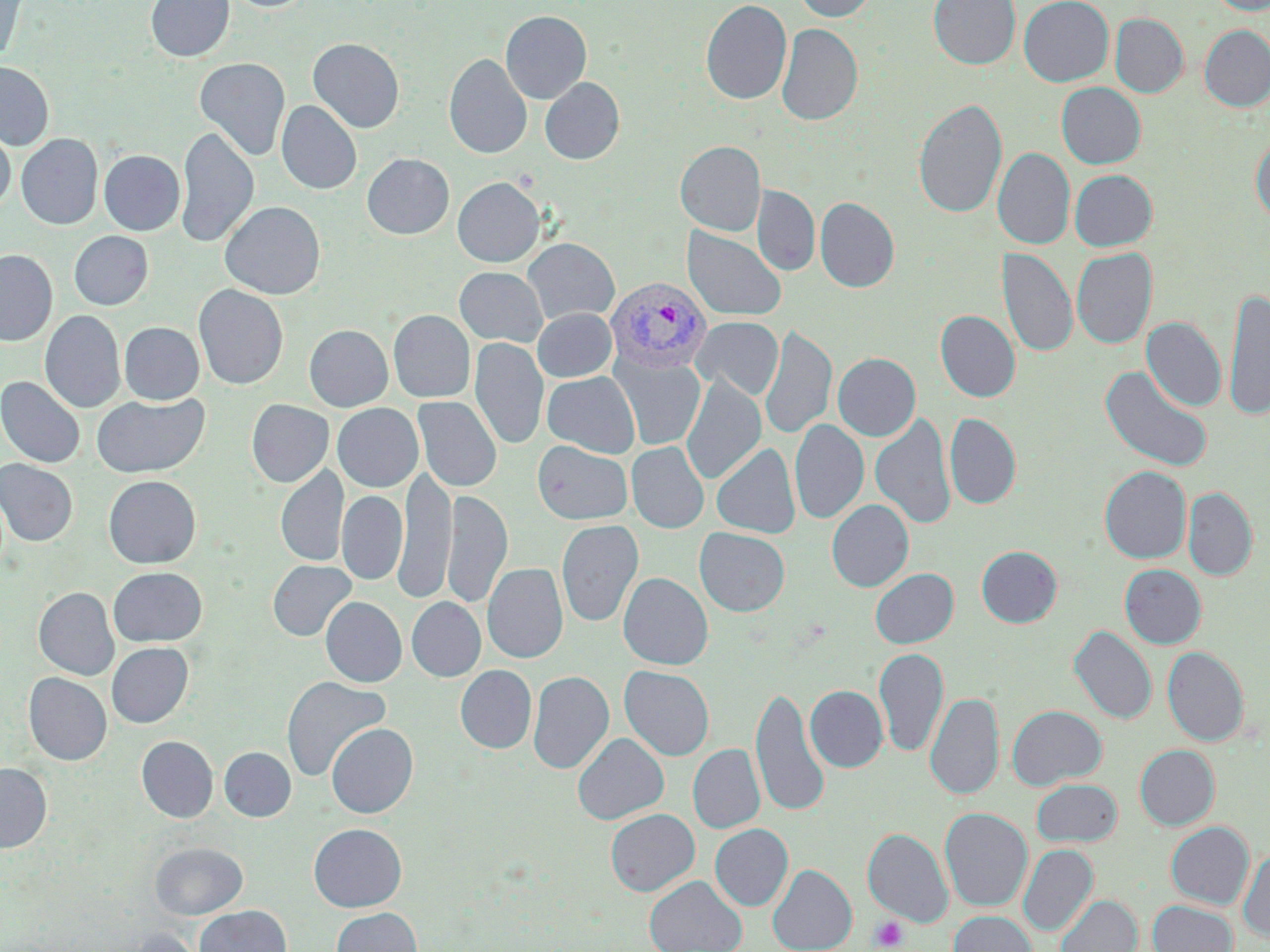
slide_level_diagnosis: Plasmodium vivax
uninfected_red_blood_cell_locations: 'approximate bounding boxes as [x1, y1, x2, y2] in pixels: [0, 0, 28, 64], [146, 0, 234, 62], [223, 0, 316, 12], [792, 0, 878, 22], [929, 0, 1020, 69], [1018, 0, 1113, 87], [1207, 0, 1270, 15], [701, 1, 791, 105], [500, 11, 591, 103], [1109, 13, 1188, 98], [776, 23, 862, 126], [1199, 25, 1270, 112], [307, 38, 404, 133], [443, 53, 532, 159], [193, 57, 291, 160], [0, 62, 54, 150], [540, 77, 624, 164], [1056, 82, 1146, 169], [913, 98, 1007, 218], [276, 101, 361, 194], [175, 125, 259, 248], [0, 127, 15, 211], [1250, 133, 1270, 224], [16, 134, 102, 229], [675, 141, 765, 236], [993, 148, 1075, 250], [98, 150, 184, 235], [362, 153, 454, 239], [1069, 169, 1157, 251], [452, 177, 545, 267], [752, 186, 820, 277], [815, 197, 899, 293], [220, 201, 325, 299], [682, 227, 787, 322], [69, 231, 153, 310], [522, 238, 619, 325], [1072, 247, 1157, 349], [998, 248, 1077, 357], [0, 249, 57, 346], [454, 267, 547, 347], [193, 284, 288, 390], [1223, 288, 1270, 420], [533, 308, 616, 382], [40, 310, 126, 413], [388, 310, 475, 403], [935, 310, 1020, 402], [692, 316, 783, 400], [1141, 317, 1226, 412], [119, 322, 204, 404], [304, 325, 393, 411], [760, 325, 837, 440], [470, 337, 549, 450], [833, 353, 921, 441], [612, 355, 705, 451], [1100, 365, 1213, 473], [542, 371, 640, 458], [681, 375, 766, 485], [0, 376, 86, 469], [92, 393, 210, 478], [412, 396, 501, 493], [246, 399, 334, 487], [257, 399, 340, 567], [332, 403, 423, 492], [944, 413, 1021, 508], [870, 414, 956, 529], [789, 419, 868, 524], [533, 440, 633, 525], [626, 441, 709, 533], [711, 443, 800, 538], [0, 459, 78, 546], [276, 465, 348, 568], [1100, 465, 1191, 563], [395, 466, 455, 603], [104, 475, 201, 568], [1183, 487, 1258, 580], [337, 490, 407, 585], [442, 490, 512, 609], [827, 499, 913, 592], [556, 519, 644, 627], [694, 527, 790, 617], [976, 545, 1062, 627], [267, 560, 356, 641], [482, 563, 568, 663], [1120, 564, 1206, 648], [108, 566, 207, 646], [870, 568, 958, 648], [618, 572, 712, 670], [33, 587, 119, 680], [321, 596, 407, 687], [406, 597, 485, 682], [1069, 625, 1157, 724], [106, 642, 193, 728], [1163, 646, 1249, 746], [874, 647, 948, 758], [455, 665, 537, 753], [619, 665, 714, 761], [528, 670, 614, 774], [24, 672, 111, 765], [281, 675, 391, 781], [749, 684, 829, 817], [805, 685, 888, 772], [925, 692, 1003, 800], [1007, 705, 1106, 789], [326, 722, 418, 818], [573, 733, 669, 825], [136, 736, 218, 822], [688, 744, 765, 833], [1135, 744, 1219, 829], [219, 747, 296, 821], [0, 763, 51, 852], [1031, 778, 1122, 846], [939, 807, 1032, 911], [605, 808, 700, 896], [1166, 821, 1254, 908], [309, 823, 406, 912], [710, 824, 793, 911], [863, 828, 953, 927], [149, 841, 248, 920], [1018, 844, 1097, 936], [1238, 848, 1270, 942], [768, 864, 856, 952], [644, 875, 746, 952], [1055, 894, 1141, 952], [1148, 900, 1237, 952], [195, 905, 290, 952], [331, 907, 422, 952], [948, 911, 1037, 952], [119, 928, 208, 952]'
magnification: 1000x
stain: May-Grünwald-Giemsa
plasmodium_vivax_infected_red_blood_cell_locations: 'approximate bounding boxes as [x1, y1, x2, y2] in pixels: [605, 276, 712, 373]'
image_size: 1270×952 pixels
field_of_view: single
preparation: thin blood smear
modality: light microscopy
platelet_locations: 'approximate bounding boxes as [x1, y1, x2, y2] in pixels: [870, 915, 908, 951]'